Point out each malaria parasite.
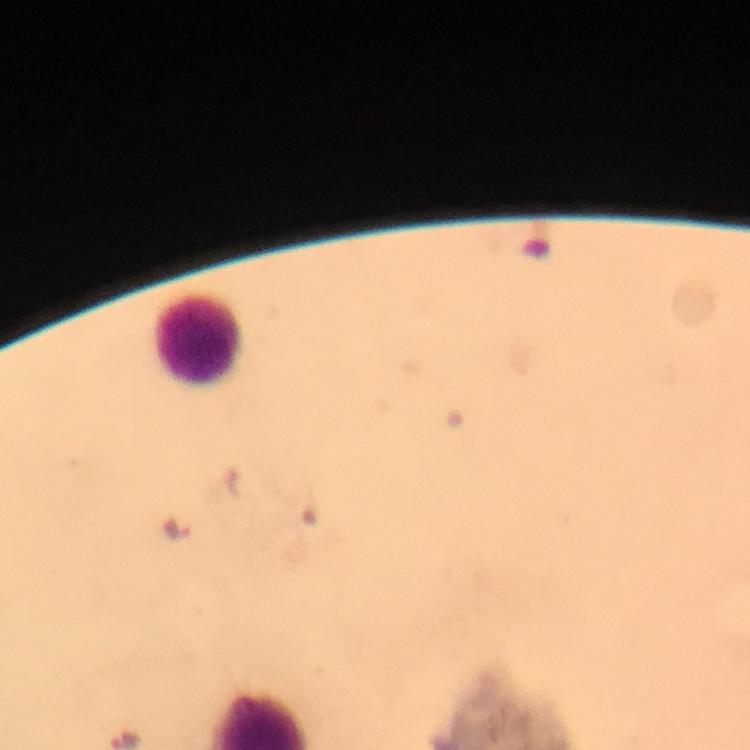
Approximate centers as {x, y} in pixels.
Malaria parasites: {179, 528}.

immersion oil = applied
capture = smartphone camera through the microscope
cropped from = one field of view
stain = Giemsa
image size = 750×750 pixels
preparation = thick blood smear
magnification = 100x
leukocyte locations = approximate centers as {x, y} in pixels: {197, 339}
context = from a malaria diagnostic workup